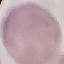 Malaria status: uninfected. Thin blood film. Photographed with a smartphone camera at the microscope eyepiece. Automatically extracted cell patch, resized to 64 × 64 pixels. Giemsa-stained preparation.